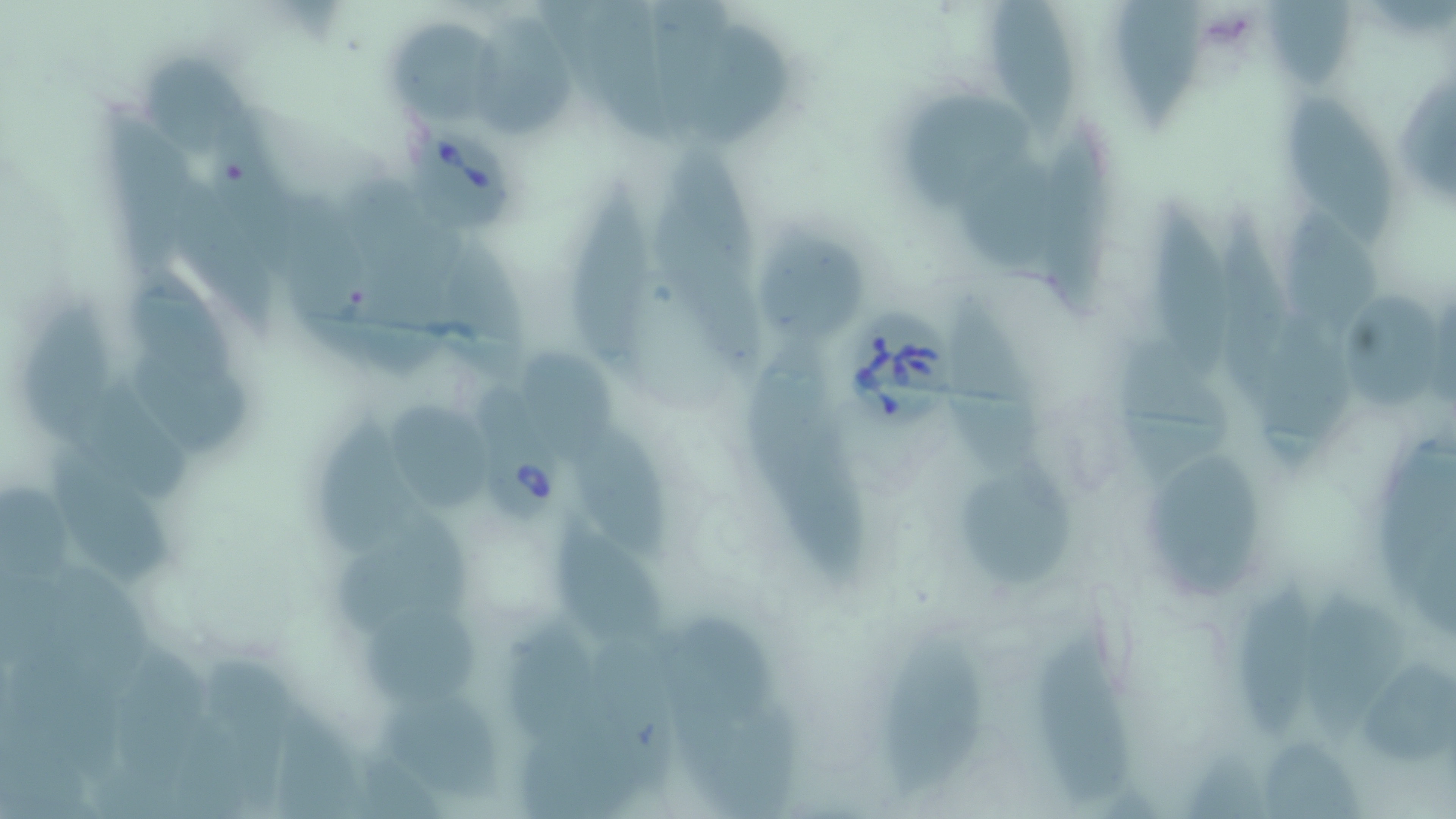
Summary:
  - Coordinate format: approximate bounding boxes as [x1, y1, x2, y2] in pixels
  - Babesia divergens-infected red blood cell locations: [404, 116, 526, 234], [839, 308, 967, 436], [461, 365, 567, 525]
  - Uninfected red blood cell locations: [579, 0, 672, 146], [984, 0, 1083, 139], [1119, 0, 1204, 130], [1266, 1, 1361, 90], [645, 2, 728, 139], [462, 13, 575, 137], [389, 15, 503, 122], [689, 23, 788, 153], [135, 57, 269, 164], [904, 90, 1032, 208], [1282, 92, 1400, 251], [91, 99, 205, 290], [1042, 131, 1121, 318], [956, 143, 1064, 276], [653, 147, 767, 381], [336, 174, 464, 383], [562, 175, 662, 389], [169, 178, 283, 343], [280, 188, 377, 357], [1140, 194, 1240, 379], [1278, 196, 1384, 346], [1208, 197, 1295, 394], [759, 233, 866, 344], [437, 244, 542, 378], [127, 275, 244, 390], [942, 289, 1062, 503], [1333, 293, 1447, 408], [23, 296, 117, 449], [1259, 311, 1357, 479], [1115, 336, 1240, 489], [745, 340, 873, 590], [515, 346, 626, 465], [127, 351, 256, 461], [58, 383, 197, 505], [389, 397, 499, 519], [318, 414, 429, 555], [568, 423, 673, 567], [42, 442, 174, 590], [1138, 449, 1266, 597], [965, 452, 1078, 591], [331, 512, 479, 639], [550, 520, 668, 647], [1232, 578, 1321, 743], [1310, 584, 1412, 753], [652, 610, 783, 724], [354, 614, 481, 715], [1030, 631, 1138, 806], [871, 638, 992, 806], [206, 653, 300, 819], [1358, 657, 1456, 774], [371, 690, 509, 807], [1260, 740, 1369, 819]
  - Slide-level diagnosis: Babesia divergens
  - Image size: 1456×819 pixels
  - Field of view: single
  - Stain: May-Grünwald-Giemsa
  - Preparation: thin blood smear
  - Modality: light microscopy
  - Magnification: 1000x